Name the parasite shown.
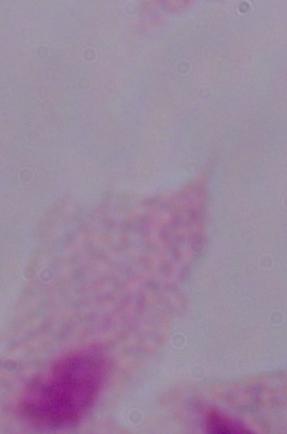

This is a trichomonad.

Summary:
  - Modality: micrograph
  - Magnification: 1000x